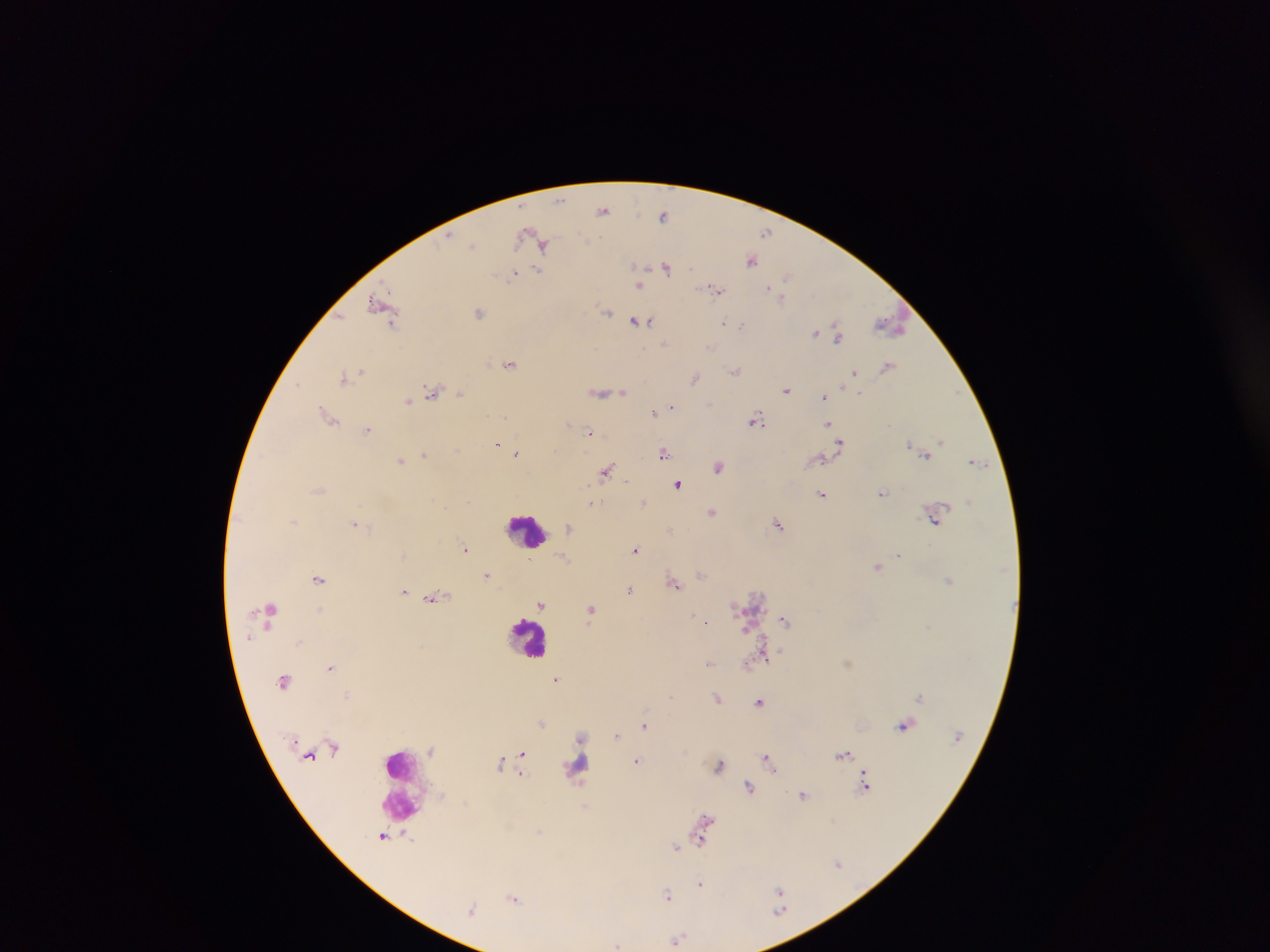

Approximate centers as {x, y} in pixels.
Summary:
  - Leukocyte locations: {527, 532}, {530, 633}, {402, 785}
  - Malaria parasite locations: {560, 198}, {604, 209}, {663, 215}, {766, 232}, {527, 235}, {449, 236}, {473, 246}, {543, 246}, {751, 259}, {637, 267}, {667, 267}, {538, 271}, {514, 273}, {788, 276}, {639, 286}, {767, 286}, {717, 290}, {381, 305}, {480, 311}, {608, 312}, {650, 321}, {392, 322}, {632, 322}, {723, 322}, {834, 322}, {640, 323}, {741, 324}, {888, 324}, {815, 332}, {837, 336}, {664, 343}, {711, 346}, {510, 362}, {888, 366}, {361, 371}, {736, 371}, {854, 371}, {342, 378}, {695, 378}, {432, 388}, {787, 390}, {461, 392}, {623, 392}, {600, 393}, {824, 397}, {409, 402}, {672, 405}, {654, 412}, {331, 421}, {756, 422}, {829, 422}, {370, 431}, {590, 432}, {940, 440}, {840, 442}, {497, 445}, {908, 445}, {517, 453}, {424, 454}, {663, 454}, {927, 455}, {402, 462}, {719, 467}, {607, 470}, {676, 484}, {318, 488}, {883, 494}, {822, 495}, {592, 504}, {447, 508}, {713, 512}, {933, 521}, {354, 523}, {779, 525}, {569, 527}, {671, 530}, {465, 548}, {637, 549}, {898, 556}, {878, 566}, {702, 575}, {487, 576}, {319, 579}, {948, 581}, {676, 584}, {630, 589}, {404, 591}, {434, 598}, {542, 605}, {271, 608}, {322, 608}, {736, 609}, {593, 610}, {698, 616}, {706, 621}, {785, 621}, {927, 627}, {298, 641}, {764, 656}, {750, 662}, {848, 662}, {710, 663}, {330, 668}, {557, 679}, {347, 694}, {671, 695}, {718, 698}, {759, 702}, {544, 723}, {644, 725}, {901, 725}, {617, 736}, {581, 737}, {430, 750}, {522, 752}, {844, 754}, {767, 757}, {501, 760}, {639, 761}, {720, 766}, {863, 772}, {579, 781}, {750, 786}, {867, 789}, {803, 795}, {585, 805}, {706, 818}, {703, 826}, {539, 831}, {385, 836}, {703, 840}, {677, 846}, {836, 861}, {702, 882}, {779, 890}, {669, 895}, {515, 898}, {678, 938}, {617, 944}
  - Preparation: thick blood film
  - Country: Ghana
  - Image size: 1270×952 pixels
  - Field of view: single
  - Capture: mobile-phone photograph through a microscope